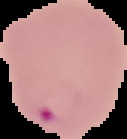

Summary:
  - Image type: segmented cell region with the area outside set to black
  - Image size: 127×139 pixels
  - Preparation: thin blood smear
  - Malaria status: parasitized